Report the malaria status of this cell.
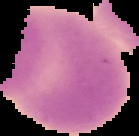

Uninfected.

{
  "image_type": "cell region segmented out of the field of view; surrounding area masked to black",
  "image_size": "139×136 pixels",
  "preparation": "thin blood smear"
}